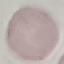

Summary:
  - Malaria status: uninfected
  - Capture: smartphone camera at the microscope eyepiece
  - Image type: cell patch, automatically extracted from a larger field of view and resized to 64 × 64 pixels
  - Preparation: thin smear
  - Stain: Giemsa